Assess the morphology of the red blood cells.
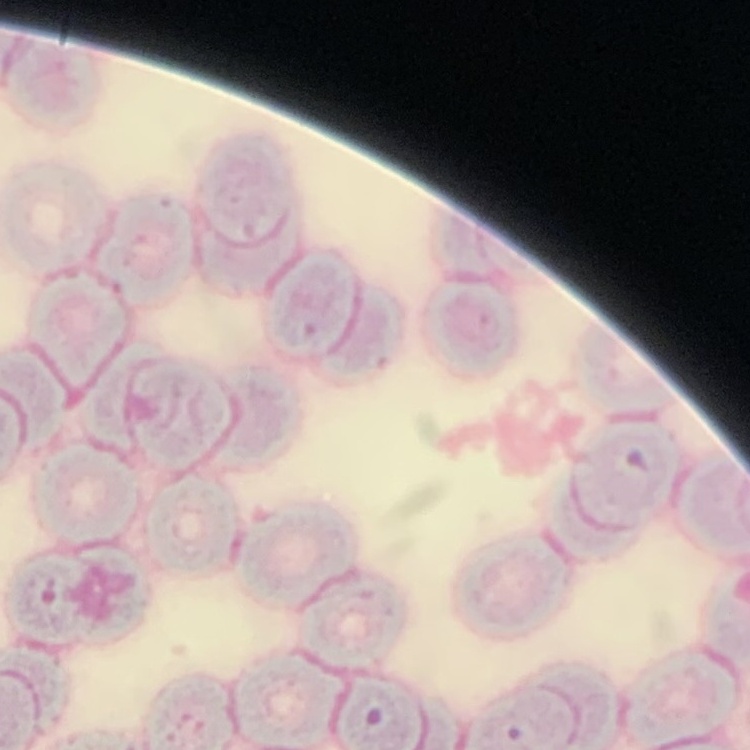

Rouleaux formation.

Summary:
  - Stain: Field's or Giemsa
  - Preparation: thin peripheral smear
  - Image type: square crop of a larger photomicrograph